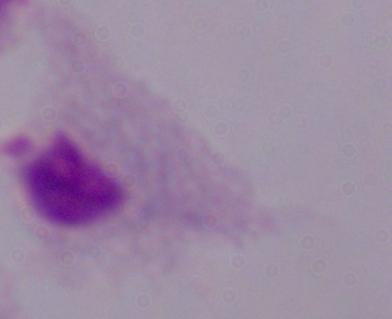
Photomicrograph. A trichomonad is shown. 1000x magnification.